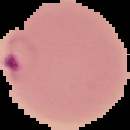

preparation = thin blood film
image size = 130×130 pixels
image type = segmented cell region with the area outside set to black
malaria status = parasitized